Locate and identify every blood parasite.
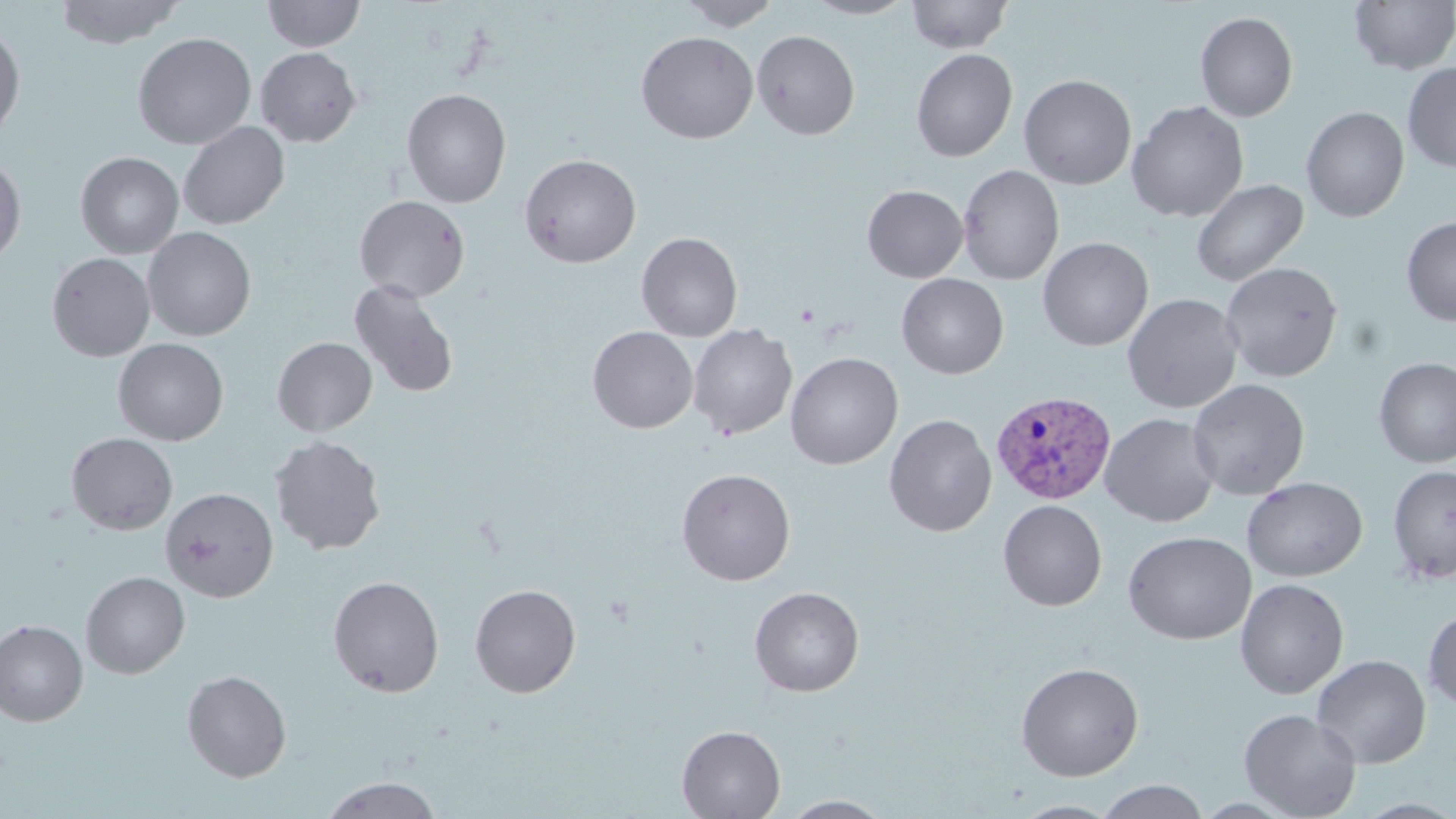

Approximate bounding boxes as [x1, y1, x2, y2] in pixels.
Plasmodium vivax-infected red blood cells: [991, 389, 1117, 504].
No Plasmodium falciparum, Plasmodium ovale, Plasmodium malariae, Babesia divergens, or Trypanosoma brucei observed.

slide_level_diagnosis: Plasmodium vivax
preparation: thin blood film
modality: light microscopy
field_of_view: single
uninfected_red_blood_cell_locations: 'approximate bounding boxes as [x1, y1, x2, y2] in pixels: [54, 0, 185, 49], [261, 0, 366, 52], [677, 0, 781, 30], [803, 0, 917, 19], [906, 0, 1013, 53], [1349, 1, 1456, 74], [1195, 11, 1298, 122], [0, 22, 26, 141], [752, 30, 860, 140], [635, 31, 759, 144], [132, 32, 257, 150], [255, 47, 361, 147], [911, 49, 1017, 162], [1402, 62, 1456, 173], [1019, 74, 1137, 190], [402, 88, 512, 207], [1127, 100, 1249, 222], [1301, 106, 1409, 222], [178, 121, 290, 230], [75, 151, 184, 259], [0, 153, 26, 267], [519, 153, 641, 267], [958, 164, 1064, 285], [1191, 178, 1308, 287], [862, 185, 968, 282], [354, 195, 470, 302], [1401, 216, 1456, 326], [142, 226, 256, 341], [637, 232, 742, 341], [1038, 237, 1153, 351], [47, 252, 155, 361], [1219, 261, 1343, 382], [896, 273, 1008, 379], [349, 280, 459, 398], [1122, 293, 1243, 413], [688, 324, 797, 440], [587, 326, 698, 433], [272, 337, 377, 436], [114, 338, 228, 445], [785, 352, 903, 469], [1373, 357, 1456, 468], [1188, 378, 1310, 500], [1100, 413, 1221, 527], [884, 414, 997, 537], [66, 433, 178, 535], [269, 435, 386, 555], [1388, 464, 1456, 584], [677, 468, 796, 585], [1242, 477, 1368, 582], [160, 487, 278, 602], [998, 499, 1107, 611], [1123, 531, 1256, 645], [81, 571, 190, 679], [328, 575, 444, 697], [1234, 578, 1349, 699], [470, 583, 581, 698], [749, 586, 864, 697], [1423, 609, 1456, 710], [0, 620, 88, 726], [1311, 654, 1431, 768], [1015, 661, 1144, 781], [182, 670, 292, 782], [1238, 708, 1362, 819], [676, 724, 786, 818], [321, 776, 442, 819], [1094, 780, 1210, 818], [779, 795, 895, 818], [1012, 799, 1121, 818]'
stain: May-Grünwald-Giemsa
magnification: 1000x
image_size: 1456×819 pixels